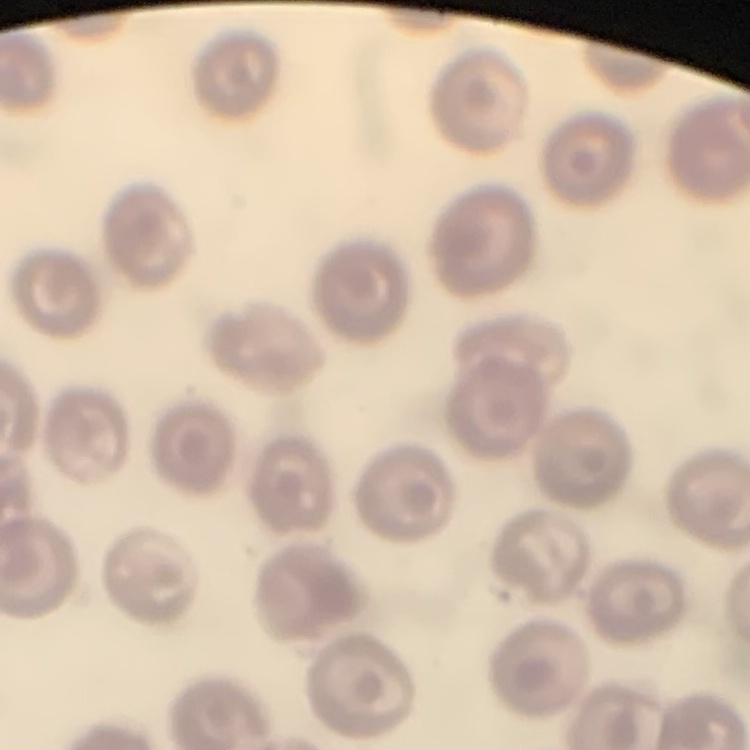

red_blood_cell_morphology: no rouleaux formation
image_type: one tile cut from a larger photomicrograph
preparation: thin blood film
stain: Field's or Giemsa